Assess this cell for malaria.
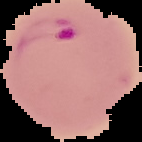
Parasitized.

image size = 142×142 pixels
image type = cell region segmented out of the field of view; surrounding area masked to black
preparation = thin blood film